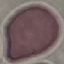

malaria status = uninfected
preparation = thin blood smear
image type = automatically extracted cell patch, resized to 64 × 64 pixels
stain = Giemsa
capture = smartphone through the microscope eyepiece